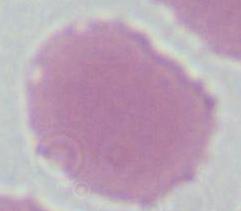

modality = micrograph
identification = red blood cell
magnification = 1000x